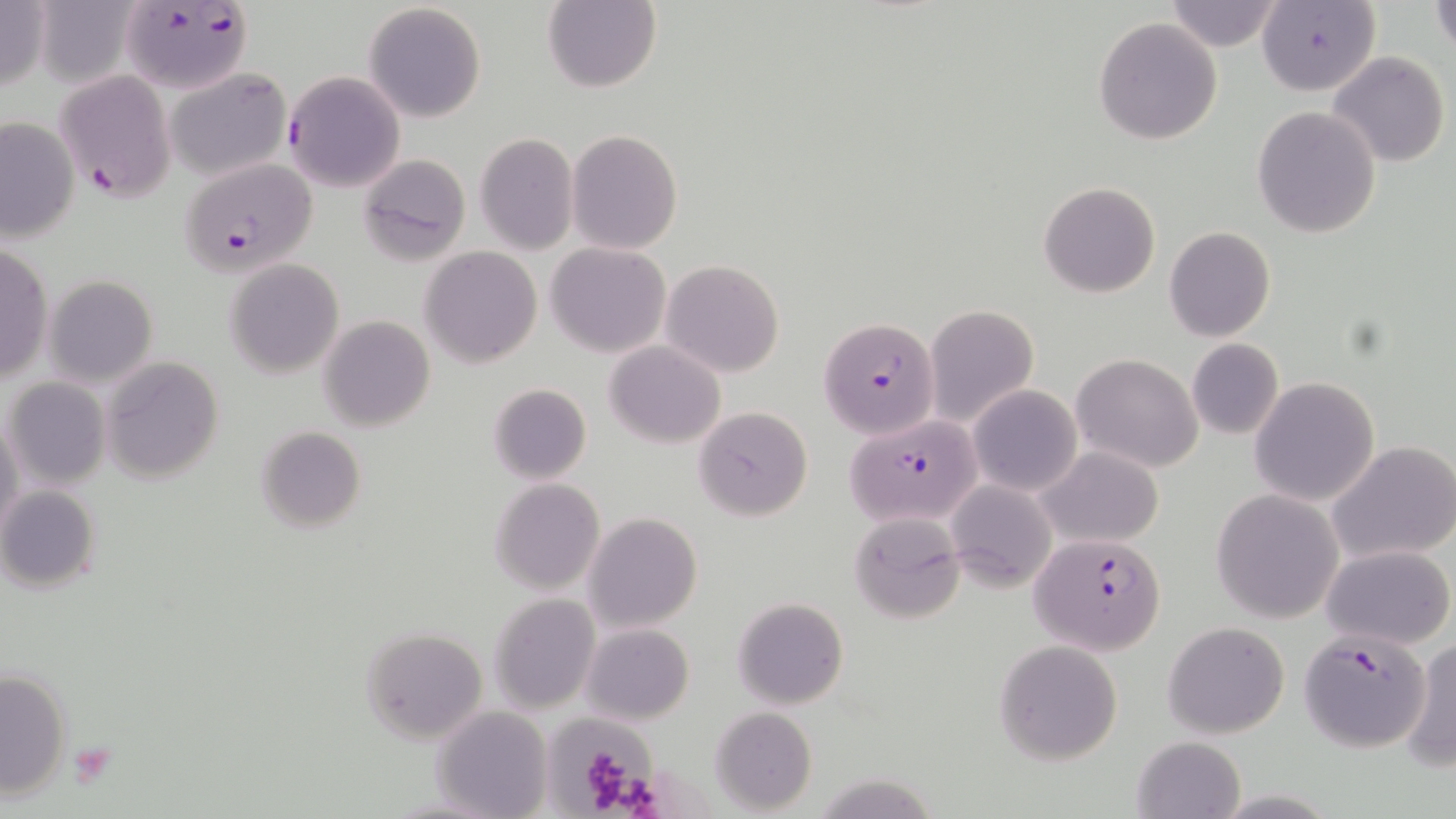
Summary:
  - Coordinate format: approximate bounding boxes as [x1, y1, x2, y2] in pixels
  - Plasmodium falciparum-infected red blood cell locations: [120, 2, 252, 95], [53, 69, 178, 201], [176, 158, 318, 277], [818, 318, 942, 438], [830, 414, 983, 538], [1031, 532, 1168, 654], [1298, 629, 1431, 753]
  - Platelet locations: [70, 740, 117, 785]
  - Uninfected red blood cell locations: [0, 0, 51, 95], [1164, 0, 1285, 52], [1432, 0, 1455, 57], [540, 1, 661, 92], [1257, 2, 1379, 97], [363, 3, 488, 121], [1093, 16, 1223, 145], [1327, 50, 1451, 167], [162, 66, 293, 182], [284, 71, 405, 192], [1251, 106, 1381, 238], [0, 114, 80, 244], [567, 129, 683, 255], [474, 133, 578, 254], [356, 154, 470, 267], [1038, 181, 1161, 299], [1163, 226, 1276, 343], [0, 239, 51, 386], [546, 243, 671, 357], [420, 246, 542, 367], [223, 259, 344, 378], [660, 259, 785, 379], [44, 276, 157, 389], [923, 304, 1039, 431], [318, 315, 435, 431], [1186, 339, 1283, 439], [605, 341, 726, 448], [1071, 353, 1203, 473], [102, 356, 224, 484], [6, 377, 109, 488], [1250, 377, 1380, 506], [488, 382, 592, 483], [969, 385, 1082, 497], [693, 406, 815, 520], [0, 408, 24, 546], [254, 426, 367, 533], [1328, 441, 1456, 566], [1037, 446, 1164, 547], [489, 478, 606, 594], [944, 480, 1057, 591], [1, 485, 103, 592], [1212, 491, 1344, 624], [583, 512, 702, 632], [848, 512, 965, 623], [1323, 544, 1455, 649], [488, 592, 601, 714], [732, 597, 848, 709], [1162, 621, 1290, 738], [581, 622, 695, 725], [360, 626, 490, 743], [1400, 638, 1456, 772], [995, 640, 1124, 767], [0, 668, 73, 798], [431, 706, 551, 819], [709, 707, 817, 815], [550, 718, 656, 813], [1132, 735, 1246, 818], [810, 772, 942, 819]
  - Slide-level diagnosis: Plasmodium falciparum
  - Stain: May-Grünwald-Giemsa
  - Image size: 1456×819 pixels
  - Magnification: 1000x
  - Preparation: thin blood smear
  - Modality: optical microscopy
  - Field of view: single